Report the malaria status of this cell.
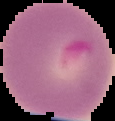

It is parasitized.

Image is 115×121 pixels. Segmented cell region on a black background. From a thin blood smear.